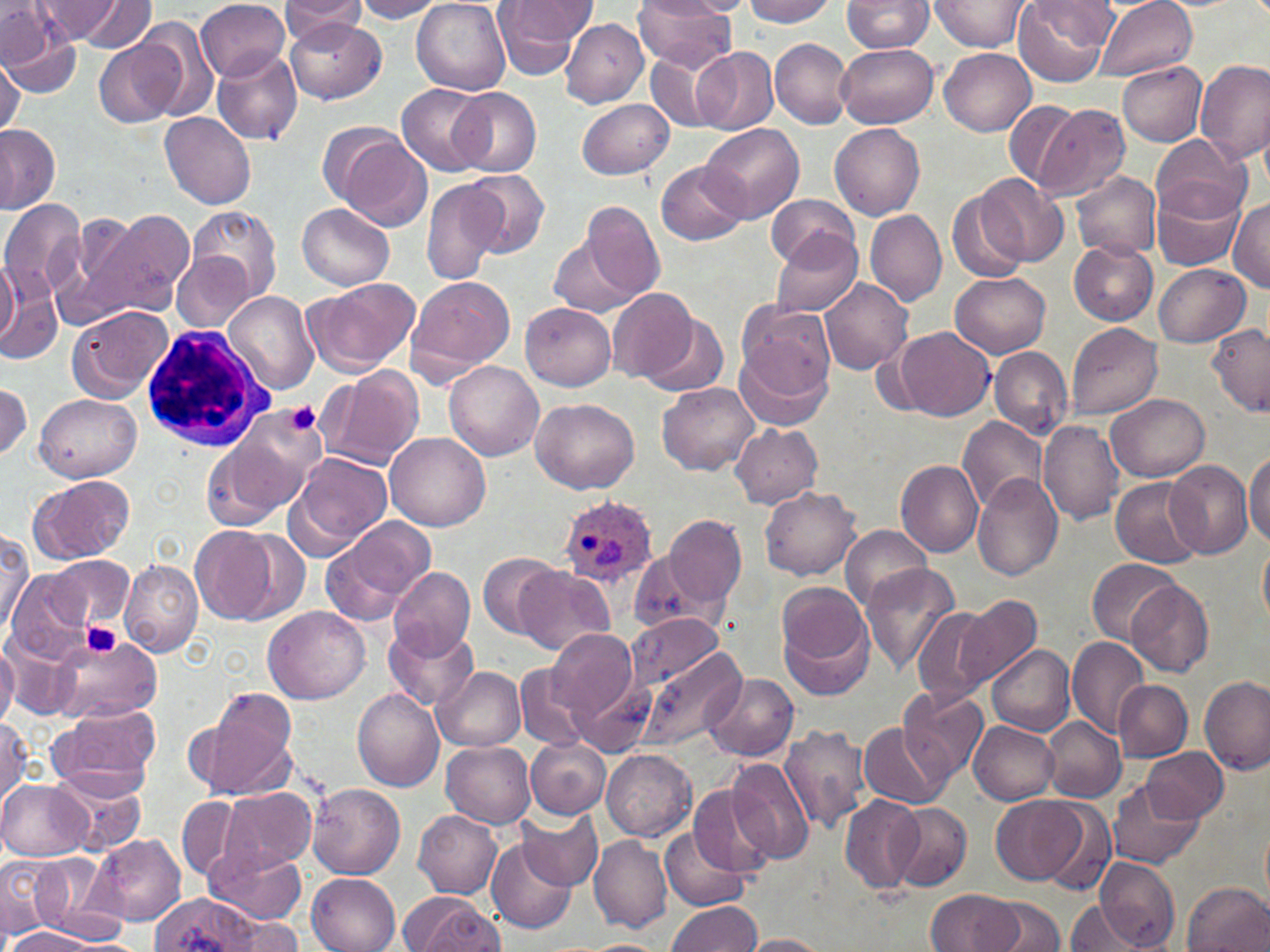
Approximate bounding boxes as named x1/y1/x2/y2 corners in pixels. Plasmodium ovale-infected red blood cell locations: (x1=559, y1=496, x2=657, y2=587). White blood cell locations: (x1=144, y1=327, x2=278, y2=454). Platelet locations: (x1=285, y1=401, x2=322, y2=434), (x1=80, y1=621, x2=123, y2=659). Uninfected red blood cell locations: (x1=280, y1=0, x2=369, y2=37), (x1=353, y1=0, x2=444, y2=23), (x1=641, y1=0, x2=737, y2=22), (x1=739, y1=0, x2=835, y2=26), (x1=842, y1=0, x2=935, y2=53), (x1=1093, y1=0, x2=1198, y2=81), (x1=35, y1=1, x2=129, y2=44), (x1=81, y1=1, x2=153, y2=53), (x1=196, y1=1, x2=291, y2=81), (x1=492, y1=1, x2=589, y2=80), (x1=633, y1=1, x2=738, y2=71), (x1=929, y1=1, x2=1032, y2=52), (x1=1012, y1=1, x2=1115, y2=86), (x1=412, y1=2, x2=511, y2=95), (x1=682, y1=2, x2=754, y2=15), (x1=0, y1=4, x2=81, y2=95), (x1=134, y1=18, x2=217, y2=120), (x1=286, y1=18, x2=385, y2=105), (x1=560, y1=19, x2=649, y2=108), (x1=770, y1=39, x2=852, y2=128), (x1=95, y1=41, x2=179, y2=129), (x1=835, y1=42, x2=937, y2=128), (x1=691, y1=47, x2=780, y2=134), (x1=211, y1=48, x2=304, y2=145), (x1=939, y1=48, x2=1035, y2=136), (x1=645, y1=49, x2=728, y2=132), (x1=1, y1=56, x2=23, y2=136), (x1=1196, y1=60, x2=1269, y2=167), (x1=1118, y1=62, x2=1207, y2=146), (x1=396, y1=84, x2=490, y2=176), (x1=452, y1=87, x2=542, y2=177), (x1=578, y1=97, x2=675, y2=179), (x1=1002, y1=99, x2=1083, y2=189), (x1=1030, y1=102, x2=1130, y2=203), (x1=160, y1=112, x2=257, y2=210), (x1=698, y1=122, x2=803, y2=223), (x1=830, y1=122, x2=926, y2=219), (x1=0, y1=123, x2=59, y2=212), (x1=1152, y1=134, x2=1250, y2=221), (x1=339, y1=137, x2=435, y2=231), (x1=655, y1=159, x2=749, y2=247), (x1=465, y1=169, x2=550, y2=257), (x1=1071, y1=171, x2=1162, y2=259), (x1=976, y1=174, x2=1070, y2=266), (x1=420, y1=179, x2=506, y2=285), (x1=1150, y1=180, x2=1247, y2=272), (x1=947, y1=190, x2=1031, y2=283), (x1=1188, y1=192, x2=1270, y2=280), (x1=767, y1=194, x2=857, y2=270), (x1=0, y1=198, x2=87, y2=301), (x1=1228, y1=199, x2=1270, y2=290), (x1=298, y1=203, x2=394, y2=291), (x1=581, y1=203, x2=668, y2=302), (x1=186, y1=206, x2=280, y2=304), (x1=67, y1=209, x2=144, y2=306), (x1=84, y1=209, x2=195, y2=317), (x1=866, y1=209, x2=947, y2=307), (x1=769, y1=230, x2=863, y2=318), (x1=549, y1=237, x2=640, y2=314), (x1=1069, y1=239, x2=1159, y2=324), (x1=172, y1=250, x2=255, y2=333), (x1=1, y1=258, x2=21, y2=350), (x1=0, y1=262, x2=53, y2=363), (x1=1153, y1=264, x2=1250, y2=348), (x1=950, y1=273, x2=1051, y2=357), (x1=406, y1=276, x2=515, y2=382), (x1=304, y1=277, x2=418, y2=373), (x1=819, y1=278, x2=915, y2=375), (x1=608, y1=287, x2=701, y2=384), (x1=225, y1=290, x2=321, y2=396), (x1=737, y1=300, x2=836, y2=397), (x1=521, y1=303, x2=615, y2=390), (x1=66, y1=304, x2=174, y2=402), (x1=418, y1=308, x2=522, y2=447), (x1=638, y1=310, x2=731, y2=397), (x1=1066, y1=323, x2=1163, y2=419), (x1=1207, y1=324, x2=1268, y2=415), (x1=891, y1=327, x2=994, y2=421), (x1=735, y1=340, x2=833, y2=435), (x1=988, y1=347, x2=1071, y2=437), (x1=443, y1=360, x2=544, y2=461), (x1=317, y1=368, x2=426, y2=470), (x1=1, y1=382, x2=31, y2=460), (x1=657, y1=382, x2=760, y2=476), (x1=35, y1=393, x2=141, y2=482), (x1=1106, y1=394, x2=1210, y2=482), (x1=531, y1=399, x2=640, y2=493), (x1=229, y1=407, x2=327, y2=506), (x1=957, y1=415, x2=1049, y2=514), (x1=1039, y1=420, x2=1123, y2=524), (x1=730, y1=422, x2=822, y2=508), (x1=202, y1=429, x2=308, y2=525), (x1=385, y1=432, x2=490, y2=531), (x1=1245, y1=449, x2=1270, y2=546), (x1=287, y1=451, x2=392, y2=555), (x1=1165, y1=459, x2=1255, y2=561), (x1=896, y1=461, x2=984, y2=557), (x1=28, y1=475, x2=134, y2=565), (x1=973, y1=475, x2=1066, y2=580), (x1=1110, y1=478, x2=1206, y2=567), (x1=760, y1=487, x2=860, y2=580), (x1=664, y1=513, x2=747, y2=609), (x1=321, y1=515, x2=436, y2=625), (x1=841, y1=525, x2=933, y2=610), (x1=190, y1=526, x2=275, y2=624), (x1=0, y1=531, x2=32, y2=628), (x1=237, y1=531, x2=311, y2=622), (x1=1258, y1=534, x2=1270, y2=629), (x1=477, y1=551, x2=562, y2=641), (x1=629, y1=552, x2=718, y2=635), (x1=0, y1=553, x2=55, y2=649), (x1=44, y1=555, x2=133, y2=630), (x1=1088, y1=558, x2=1183, y2=644), (x1=120, y1=560, x2=204, y2=658), (x1=861, y1=562, x2=962, y2=670), (x1=388, y1=565, x2=476, y2=661), (x1=517, y1=565, x2=614, y2=655), (x1=7, y1=568, x2=90, y2=656), (x1=1127, y1=580, x2=1213, y2=675), (x1=776, y1=584, x2=874, y2=698), (x1=956, y1=596, x2=1042, y2=690), (x1=264, y1=606, x2=370, y2=705), (x1=912, y1=606, x2=999, y2=709), (x1=628, y1=611, x2=726, y2=691), (x1=384, y1=624, x2=479, y2=711), (x1=547, y1=629, x2=641, y2=725), (x1=2, y1=635, x2=87, y2=719), (x1=1067, y1=635, x2=1149, y2=739), (x1=51, y1=636, x2=158, y2=724), (x1=0, y1=640, x2=17, y2=730), (x1=986, y1=643, x2=1075, y2=737), (x1=634, y1=647, x2=748, y2=753), (x1=515, y1=662, x2=592, y2=751), (x1=561, y1=662, x2=655, y2=753), (x1=435, y1=666, x2=526, y2=751), (x1=702, y1=673, x2=799, y2=762), (x1=1199, y1=675, x2=1268, y2=775), (x1=1114, y1=679, x2=1191, y2=761), (x1=899, y1=687, x2=988, y2=783), (x1=352, y1=689, x2=446, y2=790), (x1=193, y1=696, x2=297, y2=799), (x1=51, y1=706, x2=161, y2=796), (x1=0, y1=716, x2=30, y2=805), (x1=1044, y1=716, x2=1126, y2=801), (x1=970, y1=721, x2=1059, y2=804), (x1=779, y1=722, x2=872, y2=834), (x1=858, y1=722, x2=949, y2=809), (x1=525, y1=738, x2=609, y2=819), (x1=440, y1=739, x2=537, y2=829), (x1=1141, y1=747, x2=1228, y2=823), (x1=602, y1=749, x2=696, y2=840), (x1=727, y1=759, x2=815, y2=866), (x1=51, y1=767, x2=149, y2=857), (x1=1107, y1=779, x2=1205, y2=870), (x1=0, y1=780, x2=91, y2=861), (x1=307, y1=782, x2=407, y2=879), (x1=685, y1=784, x2=777, y2=878), (x1=218, y1=789, x2=315, y2=872), (x1=838, y1=794, x2=925, y2=896), (x1=992, y1=794, x2=1089, y2=886), (x1=177, y1=796, x2=242, y2=880), (x1=1033, y1=798, x2=1119, y2=895), (x1=887, y1=802, x2=972, y2=892), (x1=517, y1=809, x2=602, y2=889), (x1=413, y1=811, x2=503, y2=898), (x1=660, y1=826, x2=749, y2=913), (x1=92, y1=834, x2=186, y2=925), (x1=486, y1=835, x2=576, y2=934), (x1=589, y1=835, x2=671, y2=933), (x1=208, y1=846, x2=307, y2=923), (x1=1, y1=854, x2=65, y2=938), (x1=1094, y1=857, x2=1181, y2=950), (x1=20, y1=858, x2=124, y2=944), (x1=307, y1=872, x2=400, y2=952), (x1=1182, y1=882, x2=1270, y2=952), (x1=925, y1=889, x2=1026, y2=950), (x1=152, y1=894, x2=255, y2=952), (x1=407, y1=896, x2=502, y2=951), (x1=981, y1=896, x2=1065, y2=952), (x1=1065, y1=900, x2=1147, y2=950), (x1=666, y1=902, x2=762, y2=952), (x1=224, y1=915, x2=305, y2=951), (x1=5, y1=927, x2=103, y2=951), (x1=737, y1=933, x2=833, y2=951), (x1=578, y1=939, x2=666, y2=952). Slide-level diagnosis: Plasmodium ovale. May-Grünwald-Giemsa stain. Image is 1270×952 pixels. Thin blood film. 1000x magnification. One field of a larger specimen. Light microscopy.